Outline each blood parasite and name the species.
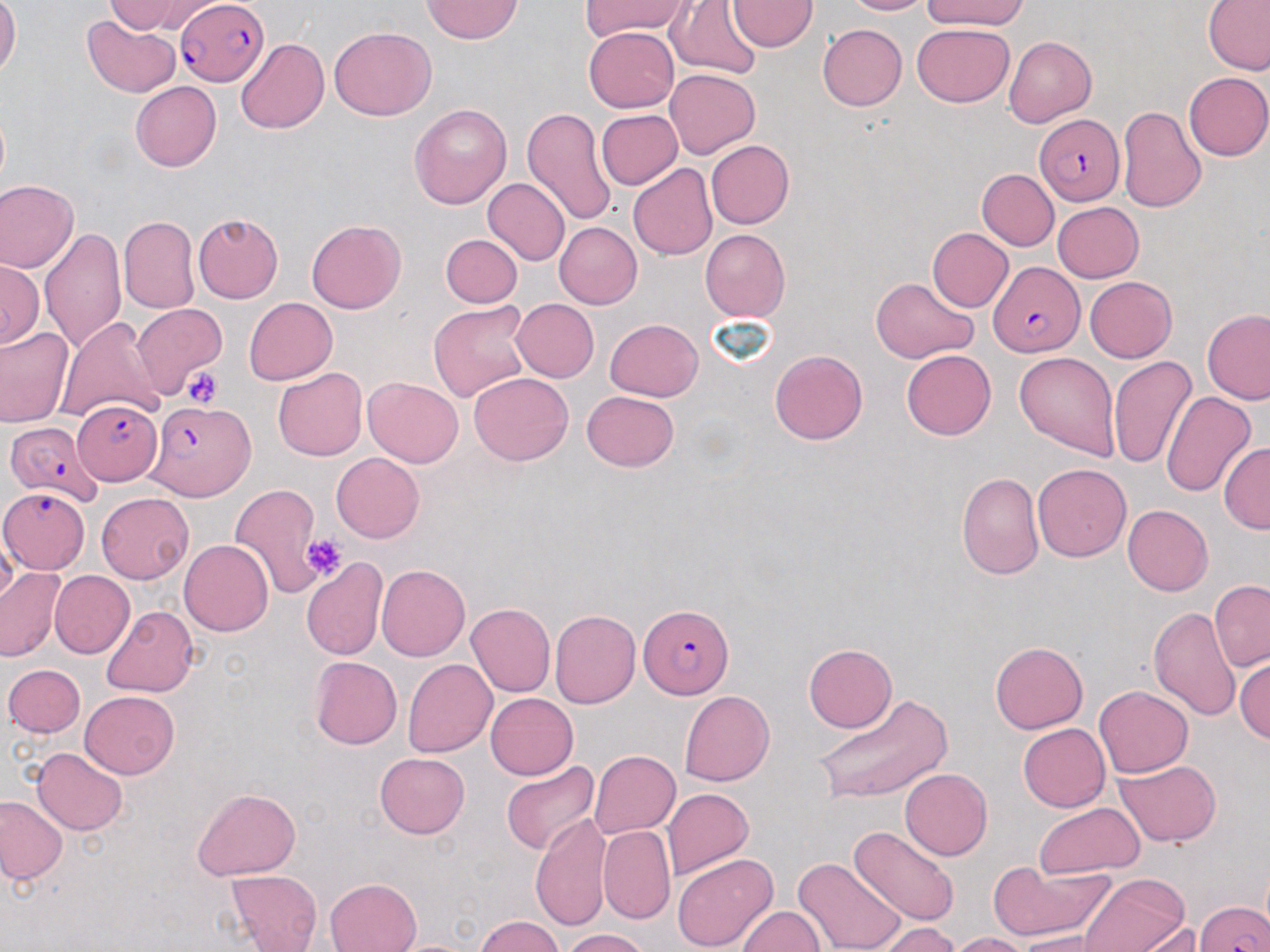

Approximate bounding boxes as (x1, y1, x2, y2) in pixels.
Plasmodium falciparum-infected red blood cells: (175, 0, 270, 86), (1035, 115, 1126, 206), (991, 261, 1083, 357), (58, 400, 161, 480), (144, 401, 255, 501), (6, 421, 105, 507), (2, 485, 91, 572), (639, 603, 733, 699), (1196, 899, 1267, 950).
No Plasmodium ovale, Plasmodium malariae, Plasmodium vivax, Babesia divergens, or Trypanosoma brucei observed.

slide-level diagnosis = Plasmodium falciparum
magnification = 1000x
stain = May-Grünwald-Giemsa
platelet locations = approximate bounding boxes as (x1, y1, x2, y2) in pixels: (180, 367, 224, 408), (301, 536, 347, 581)
image size = 1270×952 pixels
uninfected red blood cell locations = approximate bounding boxes as (x1, y1, x2, y2) in pixels: (0, 0, 21, 78), (106, 0, 207, 35), (580, 0, 692, 41), (842, 0, 932, 15), (922, 0, 1028, 29), (422, 1, 523, 43), (667, 1, 763, 80), (728, 1, 817, 52), (1202, 1, 1270, 74), (82, 14, 179, 97), (912, 22, 1015, 107), (817, 24, 906, 112), (583, 26, 679, 112), (328, 27, 437, 121), (1003, 36, 1095, 126), (235, 38, 328, 133), (666, 68, 760, 158), (1184, 71, 1269, 160), (131, 81, 222, 172), (409, 104, 511, 209), (1118, 104, 1206, 212), (521, 106, 615, 225), (596, 110, 682, 189), (706, 140, 795, 229), (628, 164, 718, 259), (978, 169, 1059, 250), (483, 178, 570, 265), (0, 179, 80, 272), (1052, 202, 1144, 283), (193, 212, 283, 303), (117, 216, 199, 313), (306, 220, 406, 313), (554, 222, 643, 309), (40, 226, 126, 355), (927, 227, 1014, 311), (699, 229, 791, 322), (440, 233, 522, 308), (0, 256, 42, 352), (869, 276, 978, 363), (1085, 277, 1176, 362), (244, 298, 336, 384), (511, 299, 599, 382), (429, 301, 534, 404), (130, 303, 228, 397), (1201, 308, 1270, 404), (55, 316, 168, 425), (605, 319, 703, 401), (0, 325, 73, 427), (770, 349, 868, 446), (901, 349, 997, 440), (1014, 351, 1121, 458), (1106, 356, 1196, 468), (273, 367, 367, 461), (469, 371, 573, 465), (362, 377, 463, 467), (581, 391, 680, 472), (1159, 391, 1256, 497), (1219, 442, 1270, 534), (331, 453, 424, 543), (1033, 463, 1131, 562), (956, 472, 1044, 580), (230, 483, 326, 597), (96, 492, 193, 584), (1122, 504, 1213, 595), (179, 539, 273, 636), (302, 558, 387, 660), (377, 563, 469, 661), (0, 566, 65, 661), (49, 571, 135, 658), (1209, 580, 1270, 671), (467, 603, 555, 697), (102, 604, 199, 697), (1148, 606, 1241, 721), (550, 610, 640, 708), (990, 641, 1088, 732), (803, 644, 896, 732), (1234, 656, 1269, 744), (310, 657, 402, 749), (403, 658, 497, 758), (3, 664, 84, 738), (1094, 685, 1192, 778), (79, 690, 180, 779), (679, 690, 774, 786), (486, 692, 578, 780), (815, 694, 952, 805), (1018, 723, 1110, 812), (30, 748, 128, 835), (589, 750, 680, 837), (376, 753, 469, 838), (1115, 758, 1221, 846), (500, 761, 600, 854), (900, 769, 993, 860), (191, 787, 301, 881), (662, 787, 753, 880), (0, 796, 67, 884), (1034, 802, 1145, 878), (530, 812, 614, 933), (598, 826, 675, 924), (849, 827, 959, 926), (603, 833, 748, 937), (672, 851, 779, 951), (793, 856, 907, 952), (988, 860, 1115, 943), (227, 869, 323, 952), (1078, 873, 1192, 952), (326, 878, 421, 952), (737, 906, 826, 951), (473, 916, 564, 952), (1122, 922, 1207, 951), (872, 923, 962, 952), (561, 928, 650, 952), (950, 932, 1032, 952), (1017, 932, 1102, 952)
modality = optical microscopy
preparation = thin blood smear
field of view = one of a larger specimen